Name the parasite shown.
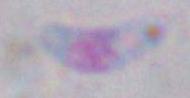

Toxoplasma gondii.

Summary:
  - Modality: photomicrograph
  - Magnification: 1000x